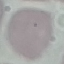
Malaria status: uninfected. Giemsa-stained preparation. Automatically extracted cell patch, resized to 64 × 64 pixels. Thin blood smear. Acquired by smartphone through the microscope eyepiece.